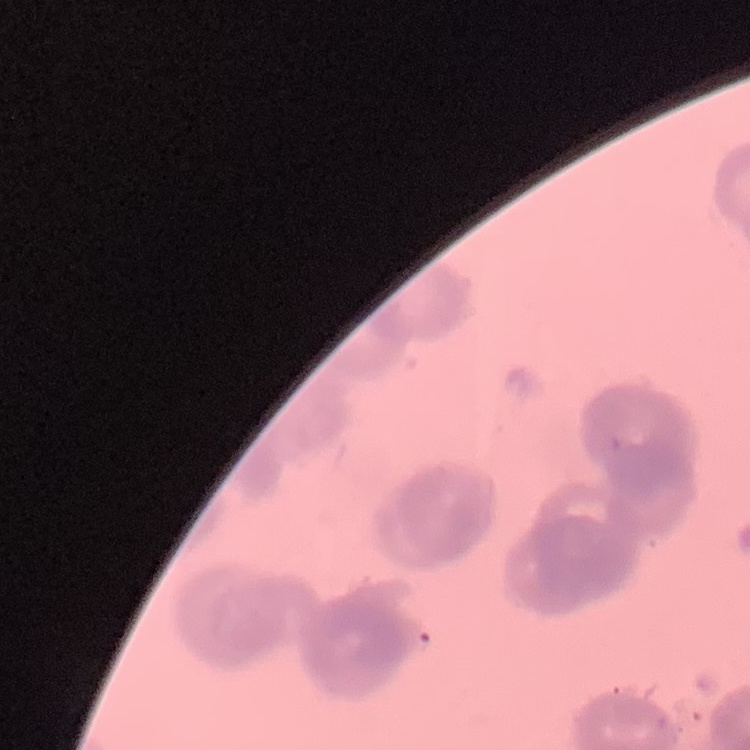

Summary:
  - Erythrocyte morphology: rouleaux formation
  - Stain: Field's or Giemsa
  - Image type: one tile cut from a larger photomicrograph
  - Preparation: thin blood film